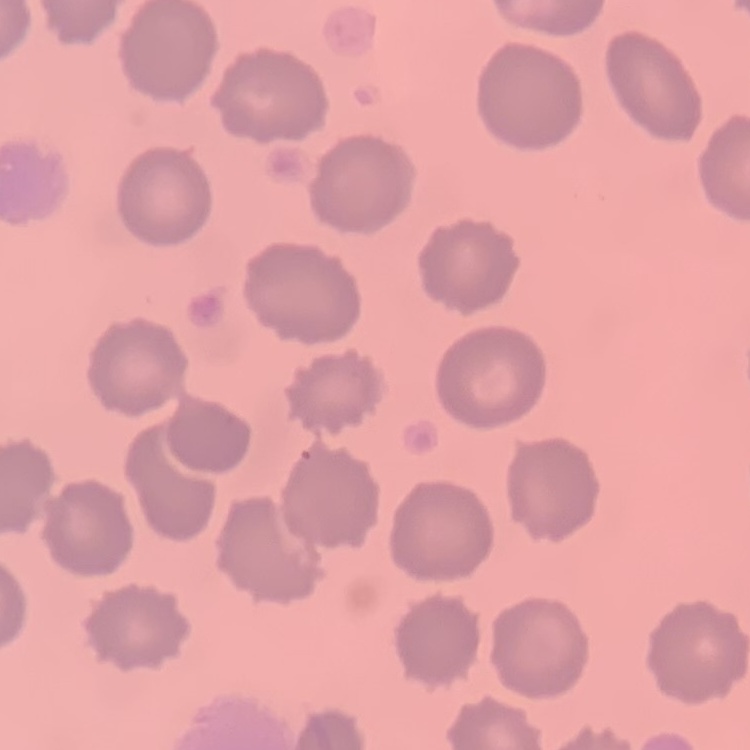

Summary:
  - Red blood cell morphology: no rouleaux formation
  - Stain: Field's or Giemsa
  - Preparation: thin blood film
  - Image type: square crop of a larger photomicrograph